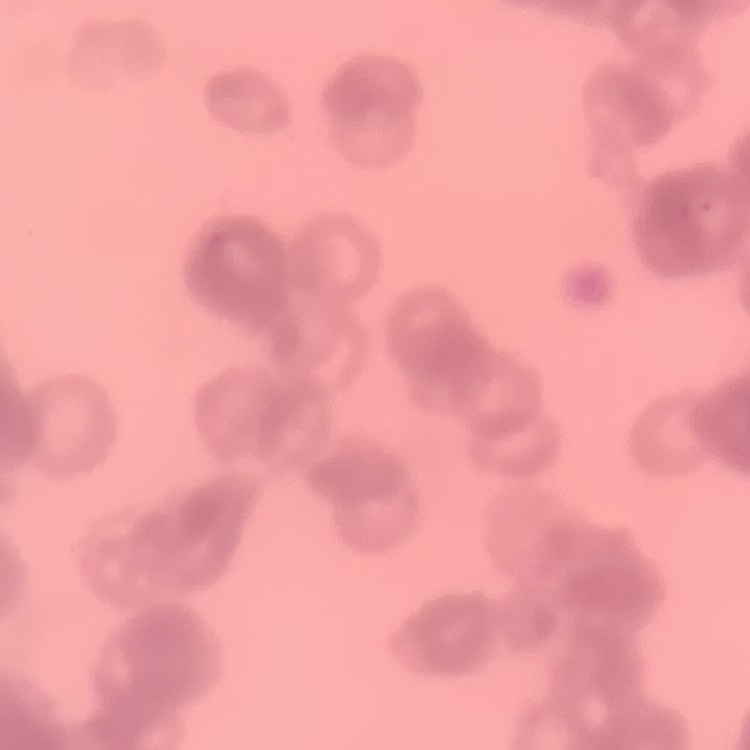
{
  "erythrocyte_morphology": "rouleaux formation",
  "preparation": "thin blood film",
  "stain": "Field's or Giemsa",
  "image_type": "square crop of a larger photomicrograph"
}